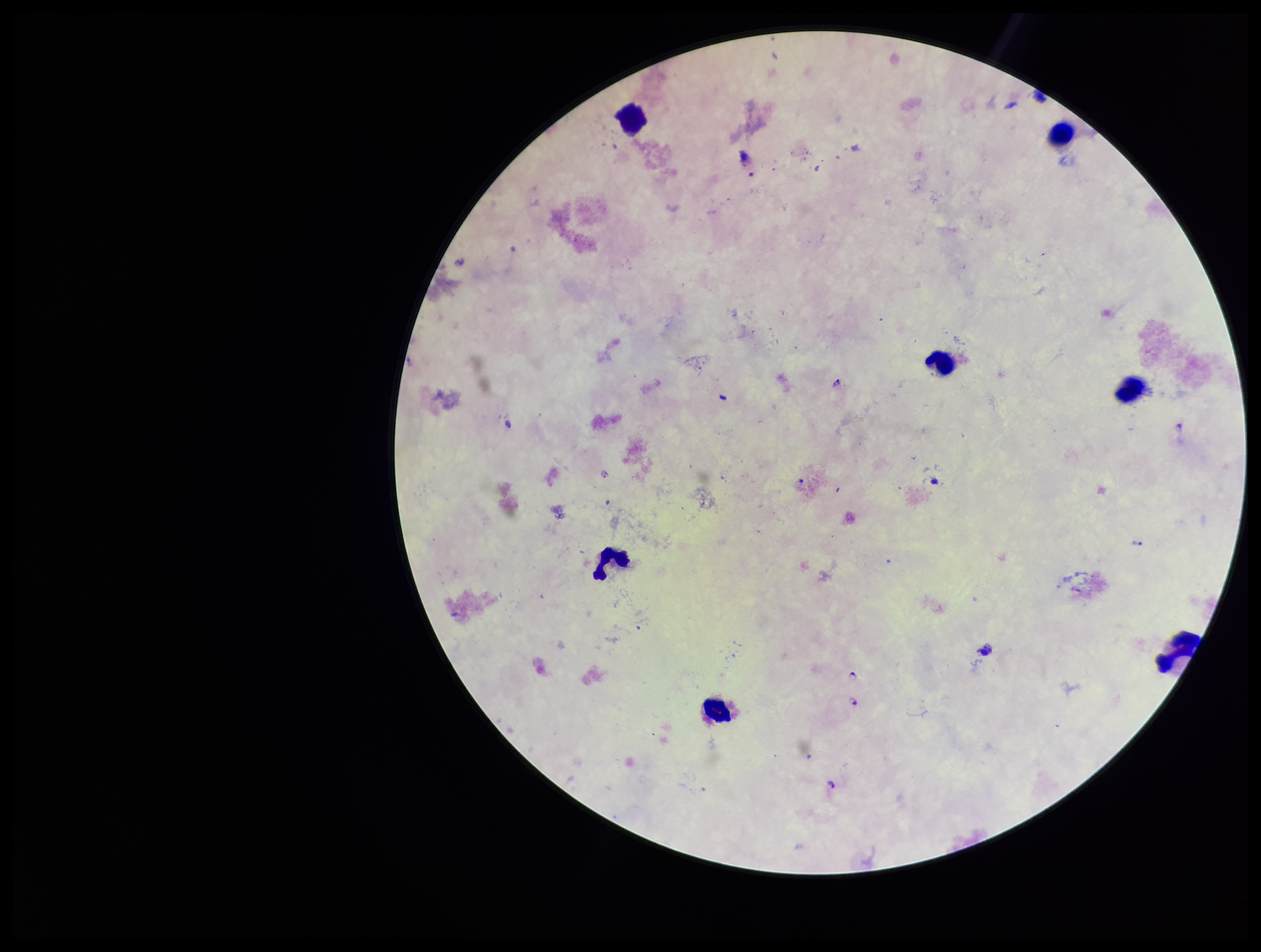
{
  "patient_malaria_status": "infected",
  "plasmodium_parasites": "seen",
  "parasite_count": 5,
  "capture": "smartphone photograph through the microscope eyepiece",
  "leukocyte_count": 7,
  "field_of_view": "single",
  "stain": "Giemsa",
  "preparation": "thick smear",
  "species_reported_for_this_patient": "Plasmodium falciparum",
  "image_size": "1261×952 pixels"
}